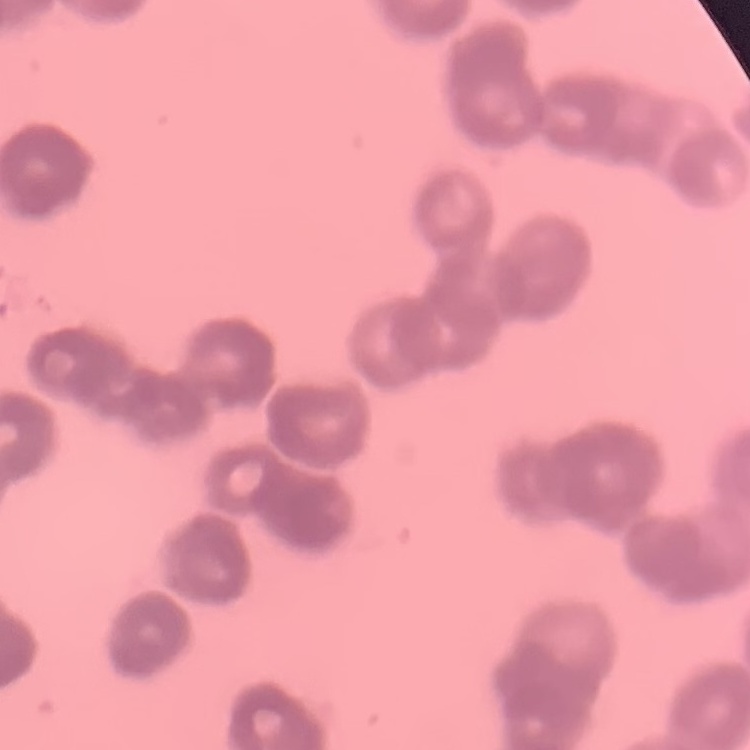 The red blood cells exhibit rouleaux formation. Square crop of a larger photomicrograph. Stained with either Field's or Giemsa. Thin peripheral smear.